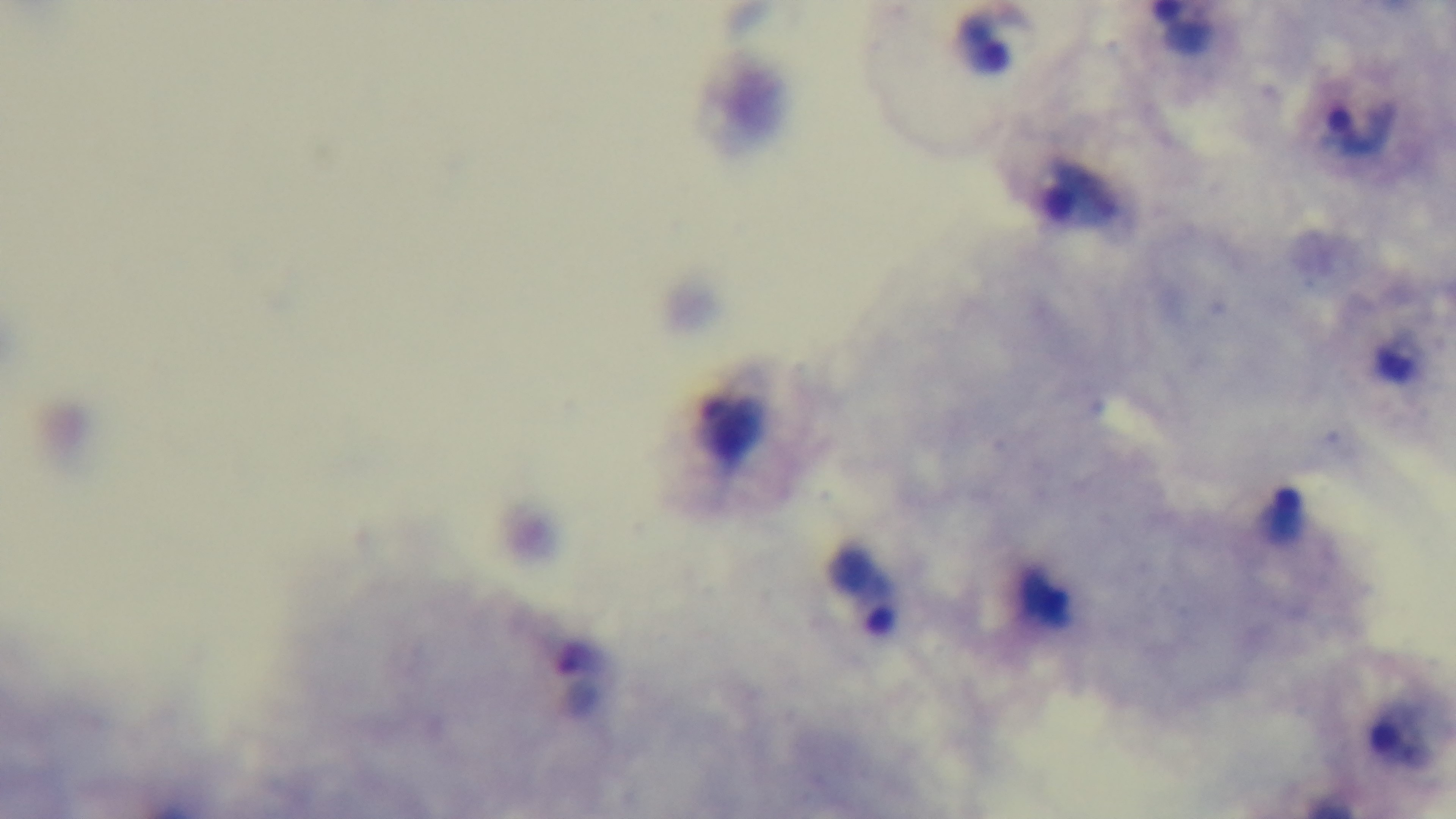
{
  "malaria_status": "positive",
  "objective": "100x oil immersion",
  "preparation": "thick smear",
  "capture": "mounted 4K digital camera",
  "modality": "light microscopy",
  "stain": "Giemsa",
  "field_of_view": "one from the slide"
}